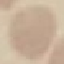

Result: no malaria parasites seen. Giemsa stain. Automatically extracted cell patch, resized to 64 × 64 pixels. Acquired by smartphone through the microscope eyepiece. Thin blood film.